Identify the parasite.
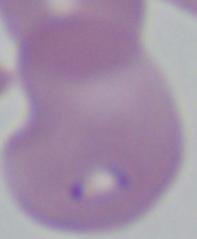

Babesia.

Summary:
  - Magnification: 1000x
  - Modality: micrograph